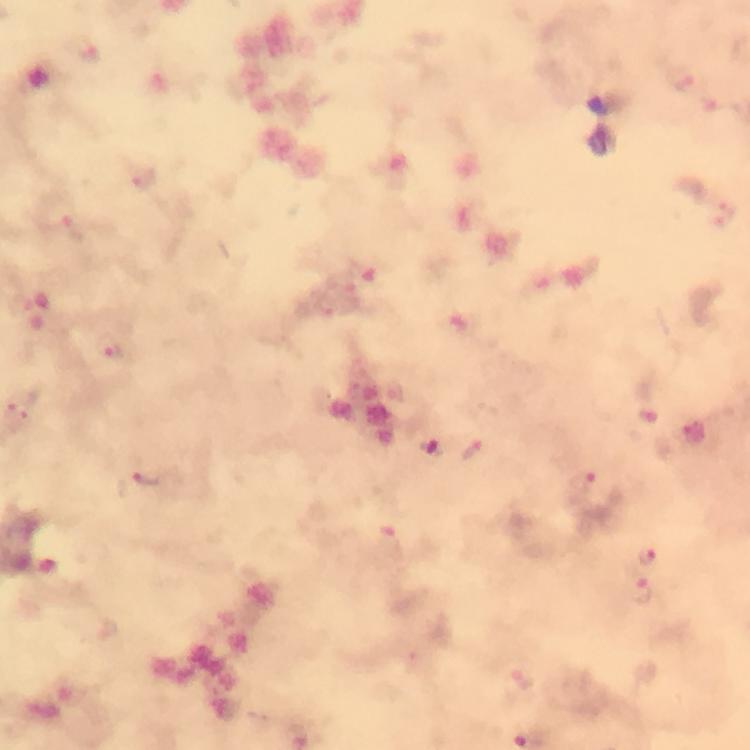

image size = 750×750 pixels
magnification = 100x
immersion oil = applied
preparation = thick blood film
cropped from = one field of view
stain = Giemsa
context = from a malaria diagnostic workup
Plasmodium parasite locations = approximate centers as (x, y) in pixels: (89, 51), (682, 77), (717, 102), (145, 179), (71, 232), (116, 352), (650, 416), (430, 448), (474, 449), (152, 479), (582, 482), (649, 556), (642, 593)
capture = smartphone mounted on the microscope